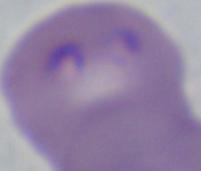
identification = Babesia
magnification = 1000x
modality = photomicrograph